State which cell type is depicted.
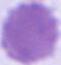
This is an erythrocyte.

Summary:
  - Modality: micrograph
  - Magnification: 1000x